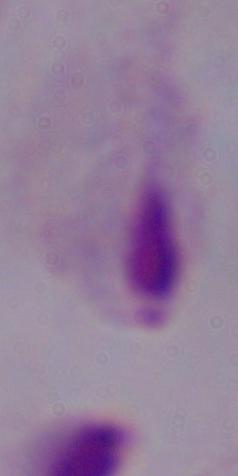

identification = trichomonad
modality = photomicrograph
magnification = 1000x